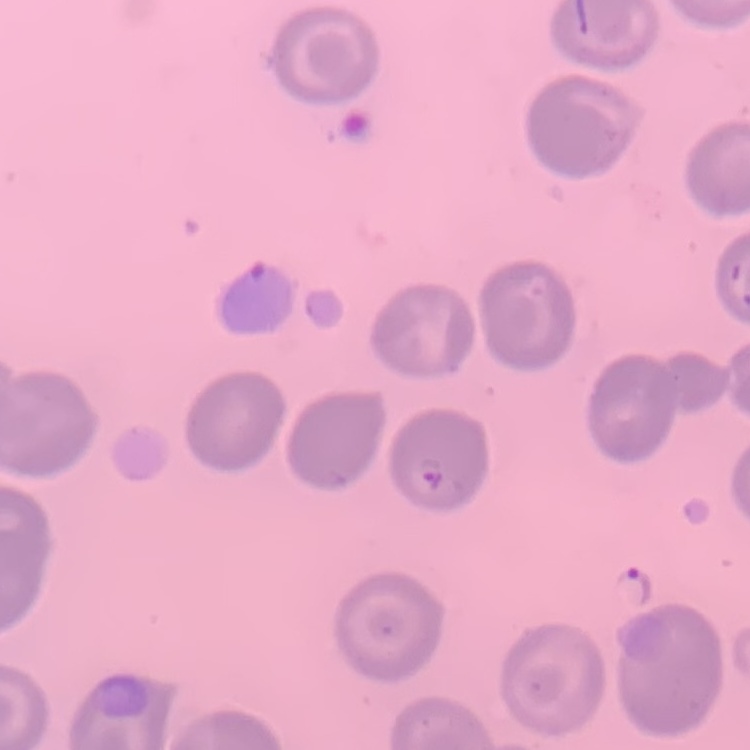

The erythrocytes show no rouleaux formation. One tile cut from a larger photomicrograph. Field's or Giemsa stain. Thin peripheral smear.